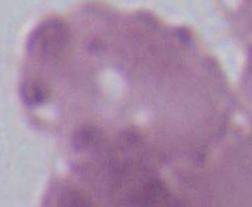
Summary:
  - Modality: photomicrograph
  - Magnification: 1000x
  - Identification: red blood cell